Outline each white blood cell.
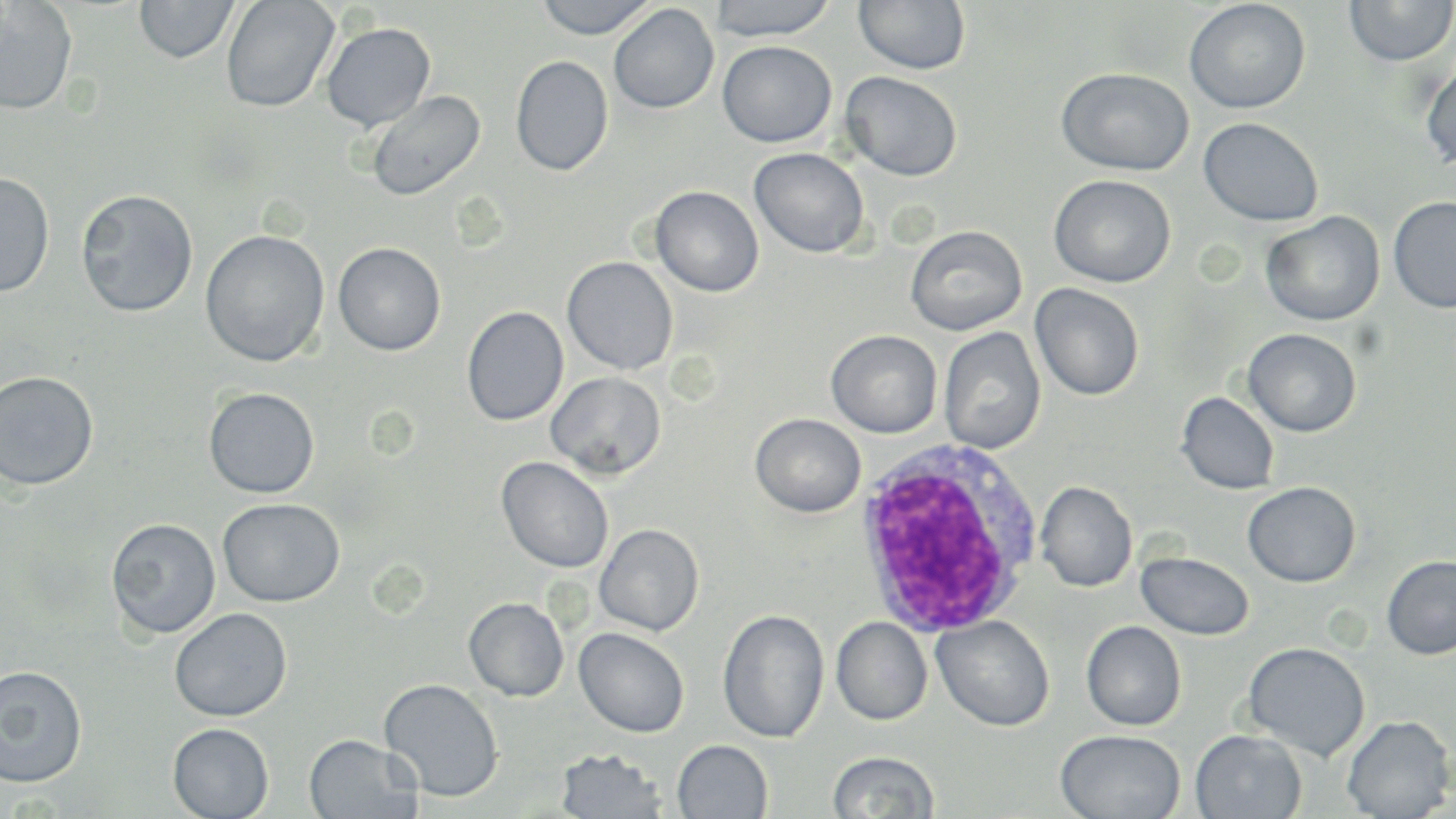

Approximate bounding boxes as named x1/y1/x2/y2 corners in pixels.
White blood cells: (x1=852, y1=438, x2=1043, y2=640).

Summary:
  - Uninfected red blood cell locations: (x1=135, y1=0, x2=240, y2=63), (x1=220, y1=0, x2=340, y2=113), (x1=533, y1=0, x2=659, y2=40), (x1=707, y1=0, x2=840, y2=42), (x1=1344, y1=0, x2=1456, y2=66), (x1=0, y1=1, x2=78, y2=116), (x1=853, y1=1, x2=971, y2=75), (x1=1184, y1=1, x2=1310, y2=114), (x1=609, y1=4, x2=720, y2=114), (x1=321, y1=22, x2=436, y2=131), (x1=717, y1=41, x2=836, y2=147), (x1=1421, y1=53, x2=1456, y2=173), (x1=510, y1=55, x2=614, y2=177), (x1=1056, y1=67, x2=1194, y2=176), (x1=840, y1=71, x2=962, y2=182), (x1=365, y1=89, x2=485, y2=201), (x1=1199, y1=117, x2=1323, y2=226), (x1=748, y1=147, x2=869, y2=258), (x1=0, y1=171, x2=55, y2=298), (x1=1048, y1=174, x2=1176, y2=288), (x1=649, y1=185, x2=764, y2=297), (x1=75, y1=188, x2=199, y2=318), (x1=1388, y1=195, x2=1456, y2=314), (x1=1261, y1=211, x2=1385, y2=326), (x1=905, y1=225, x2=1027, y2=336), (x1=200, y1=229, x2=330, y2=367), (x1=332, y1=242, x2=446, y2=356), (x1=562, y1=256, x2=679, y2=376), (x1=1030, y1=283, x2=1145, y2=401), (x1=461, y1=306, x2=568, y2=426), (x1=939, y1=327, x2=1046, y2=455), (x1=1242, y1=328, x2=1362, y2=437), (x1=826, y1=329, x2=943, y2=438), (x1=0, y1=370, x2=100, y2=491), (x1=546, y1=371, x2=666, y2=480), (x1=203, y1=387, x2=320, y2=499), (x1=1176, y1=392, x2=1279, y2=494), (x1=750, y1=413, x2=866, y2=518), (x1=496, y1=456, x2=614, y2=573), (x1=1035, y1=481, x2=1137, y2=592), (x1=1243, y1=482, x2=1360, y2=586), (x1=217, y1=498, x2=344, y2=607), (x1=106, y1=517, x2=221, y2=640), (x1=594, y1=524, x2=704, y2=636), (x1=1137, y1=551, x2=1254, y2=640), (x1=1381, y1=556, x2=1456, y2=659), (x1=464, y1=597, x2=569, y2=701), (x1=169, y1=608, x2=293, y2=722), (x1=717, y1=609, x2=829, y2=743), (x1=932, y1=615, x2=1055, y2=732), (x1=831, y1=617, x2=933, y2=725), (x1=1081, y1=620, x2=1187, y2=731), (x1=574, y1=627, x2=689, y2=738), (x1=1242, y1=641, x2=1371, y2=760), (x1=0, y1=665, x2=88, y2=788), (x1=378, y1=678, x2=504, y2=802), (x1=1342, y1=714, x2=1455, y2=819), (x1=168, y1=723, x2=274, y2=819), (x1=1055, y1=729, x2=1186, y2=818), (x1=1190, y1=729, x2=1308, y2=818), (x1=303, y1=734, x2=423, y2=819), (x1=672, y1=739, x2=773, y2=818), (x1=555, y1=748, x2=668, y2=818), (x1=827, y1=750, x2=940, y2=818)
  - Slide-level diagnosis: Plasmodium ovale
  - Magnification: 1000x
  - Field of view: single
  - Image size: 1456×819 pixels
  - Stain: May-Grünwald-Giemsa
  - Preparation: thin blood smear
  - Modality: light microscopy